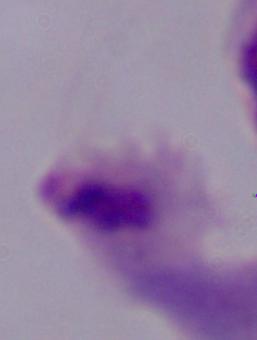
modality = photomicrograph
magnification = 1000x
identification = trichomonad